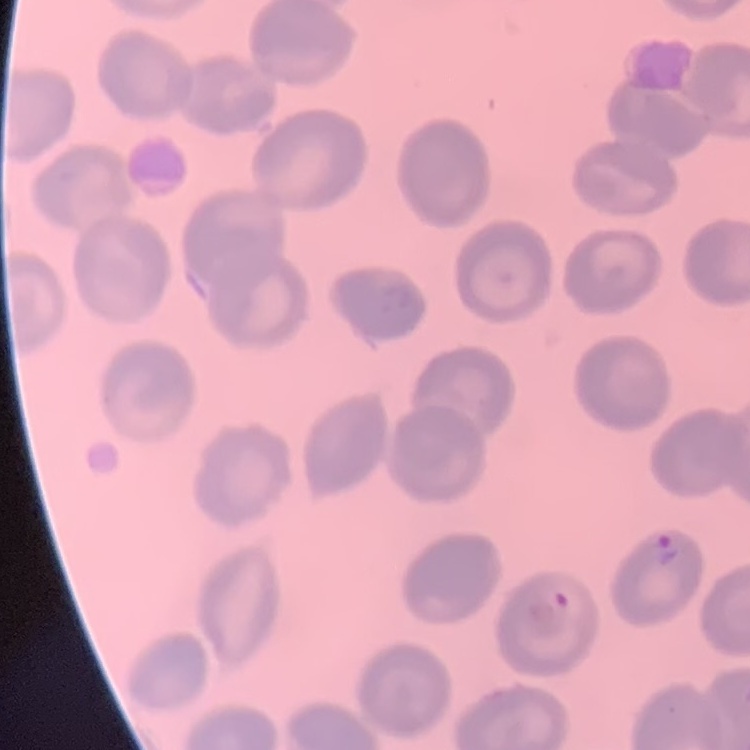

The erythrocytes show no rouleaux formation. One tile cut from a larger photomicrograph. Thin blood smear. Field's or Giemsa stain.